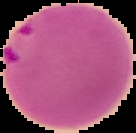 Cell region segmented out of the field of view; the surrounding area is masked to black. Malaria status: parasitized. From a thin blood film. Image is 136×133 pixels.